Locate every blood parasite and identify its species.
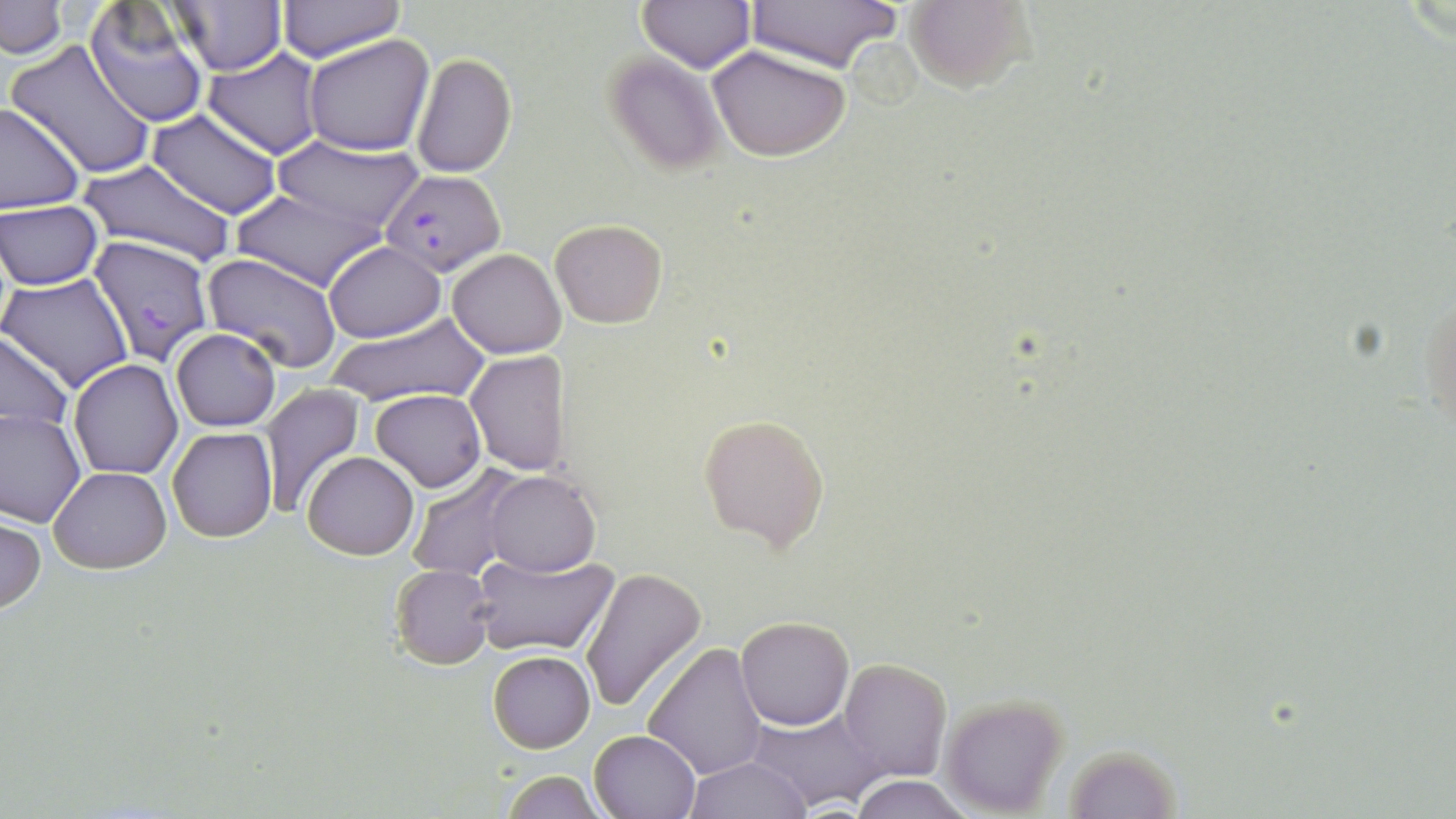

Approximate bounding boxes as [x1, y1, x2, y2] in pixels.
Plasmodium falciparum-infected red blood cells: [382, 169, 505, 276], [88, 234, 215, 363].
No Plasmodium ovale, Plasmodium malariae, Plasmodium vivax, Babesia divergens, or Trypanosoma brucei observed.

slide-level diagnosis = Plasmodium falciparum
preparation = thin blood film
image size = 1456×819 pixels
magnification = 1000x
field of view = single
uninfected red blood cell locations = approximate bounding boxes as [x1, y1, x2, y2] in pixels: [1, 0, 66, 58], [169, 0, 286, 75], [638, 0, 756, 72], [744, 0, 904, 74], [904, 0, 1032, 93], [278, 1, 405, 64], [84, 3, 212, 128], [303, 34, 434, 156], [7, 39, 156, 178], [709, 46, 851, 163], [203, 50, 324, 160], [603, 51, 726, 175], [411, 53, 515, 176], [0, 101, 85, 211], [147, 110, 282, 220], [272, 138, 425, 233], [78, 159, 236, 271], [232, 189, 383, 290], [0, 200, 104, 290], [549, 218, 667, 328], [325, 241, 444, 343], [448, 247, 567, 359], [202, 253, 344, 374], [2, 273, 135, 393], [1419, 283, 1455, 446], [323, 311, 491, 409], [170, 328, 280, 431], [0, 331, 75, 439], [464, 351, 569, 475], [68, 359, 183, 479], [259, 386, 366, 519], [372, 389, 487, 492], [0, 409, 85, 527], [700, 415, 830, 554], [167, 425, 277, 541], [302, 450, 418, 559], [406, 466, 527, 584], [49, 467, 171, 574], [485, 470, 600, 577], [0, 514, 45, 614], [470, 549, 621, 659], [390, 564, 495, 668], [581, 566, 708, 713], [735, 615, 854, 730], [643, 641, 767, 779], [488, 650, 596, 754], [839, 658, 952, 783], [939, 691, 1072, 817], [750, 709, 883, 809], [588, 729, 700, 819], [1060, 744, 1185, 817], [686, 756, 810, 818], [499, 771, 610, 818], [849, 775, 973, 819]
modality = light microscopy
stain = May-Grünwald-Giemsa